Outline each blood parasite and name the species.
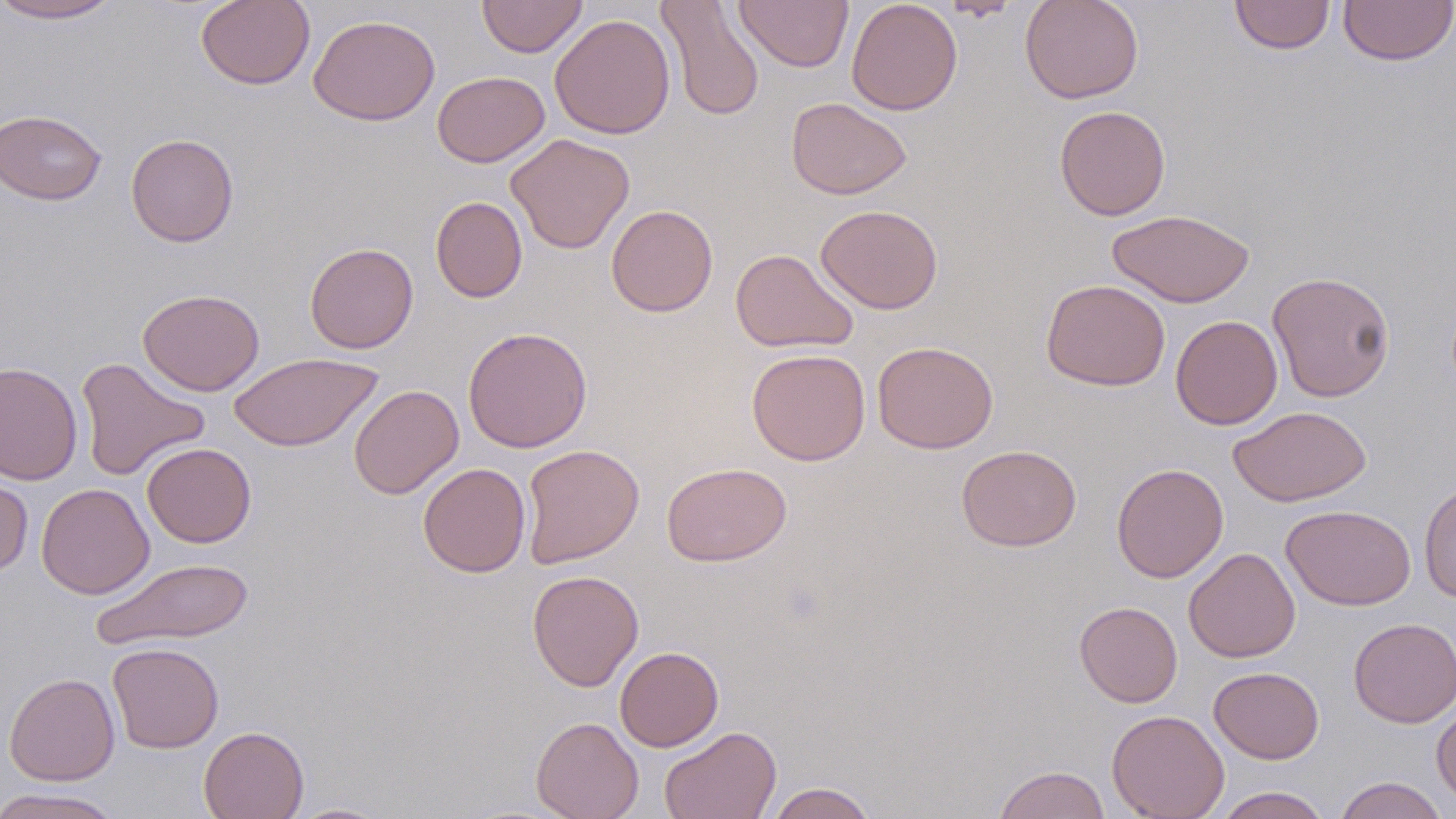

No blood parasites seen.

Approximate bounding boxes as named x1/y1/x2/y2 corners in pixels. Uninfected red blood cell locations: (x1=0, y1=0, x2=123, y2=23), (x1=477, y1=0, x2=587, y2=58), (x1=734, y1=0, x2=853, y2=72), (x1=845, y1=0, x2=963, y2=116), (x1=1019, y1=0, x2=1144, y2=104), (x1=1229, y1=0, x2=1335, y2=55), (x1=1338, y1=0, x2=1456, y2=66), (x1=196, y1=1, x2=314, y2=89), (x1=657, y1=1, x2=765, y2=121), (x1=936, y1=1, x2=1023, y2=21), (x1=550, y1=13, x2=676, y2=139), (x1=308, y1=14, x2=440, y2=126), (x1=432, y1=70, x2=550, y2=167), (x1=786, y1=97, x2=912, y2=200), (x1=1054, y1=104, x2=1171, y2=221), (x1=0, y1=109, x2=108, y2=205), (x1=125, y1=133, x2=239, y2=247), (x1=506, y1=133, x2=635, y2=254), (x1=430, y1=196, x2=528, y2=303), (x1=606, y1=204, x2=718, y2=317), (x1=816, y1=204, x2=943, y2=314), (x1=1107, y1=208, x2=1255, y2=308), (x1=305, y1=242, x2=419, y2=354), (x1=730, y1=248, x2=858, y2=353), (x1=1267, y1=270, x2=1396, y2=402), (x1=1041, y1=279, x2=1171, y2=390), (x1=138, y1=288, x2=264, y2=396), (x1=1170, y1=315, x2=1283, y2=430), (x1=463, y1=327, x2=593, y2=454), (x1=872, y1=340, x2=998, y2=454), (x1=747, y1=348, x2=871, y2=465), (x1=229, y1=352, x2=383, y2=452), (x1=75, y1=357, x2=210, y2=481), (x1=0, y1=361, x2=83, y2=486), (x1=349, y1=384, x2=464, y2=499), (x1=1228, y1=405, x2=1372, y2=507), (x1=141, y1=442, x2=256, y2=548), (x1=520, y1=443, x2=644, y2=568), (x1=956, y1=444, x2=1082, y2=551), (x1=417, y1=462, x2=531, y2=577), (x1=662, y1=462, x2=792, y2=566), (x1=1111, y1=463, x2=1228, y2=583), (x1=0, y1=469, x2=34, y2=578), (x1=36, y1=483, x2=154, y2=599), (x1=1419, y1=483, x2=1456, y2=601), (x1=1280, y1=504, x2=1416, y2=610), (x1=1184, y1=547, x2=1300, y2=663), (x1=91, y1=557, x2=255, y2=651), (x1=527, y1=569, x2=644, y2=692), (x1=1074, y1=601, x2=1182, y2=708), (x1=1348, y1=617, x2=1456, y2=728), (x1=107, y1=642, x2=224, y2=753), (x1=615, y1=646, x2=724, y2=751), (x1=1209, y1=666, x2=1324, y2=764), (x1=4, y1=672, x2=120, y2=785), (x1=1431, y1=702, x2=1456, y2=806), (x1=1106, y1=709, x2=1230, y2=819), (x1=531, y1=716, x2=644, y2=819), (x1=198, y1=726, x2=309, y2=819), (x1=659, y1=726, x2=781, y2=819), (x1=993, y1=765, x2=1111, y2=819), (x1=1332, y1=776, x2=1451, y2=819), (x1=765, y1=782, x2=878, y2=819), (x1=1213, y1=787, x2=1331, y2=819), (x1=0, y1=788, x2=119, y2=819), (x1=286, y1=802, x2=393, y2=818). Slide-level diagnosis: no evidence of blood parasites. Image is 1456×819 pixels. 1000x magnification. Optical microscopy. May-Grünwald-Giemsa-stained preparation. One field of a larger specimen. Thin blood smear.